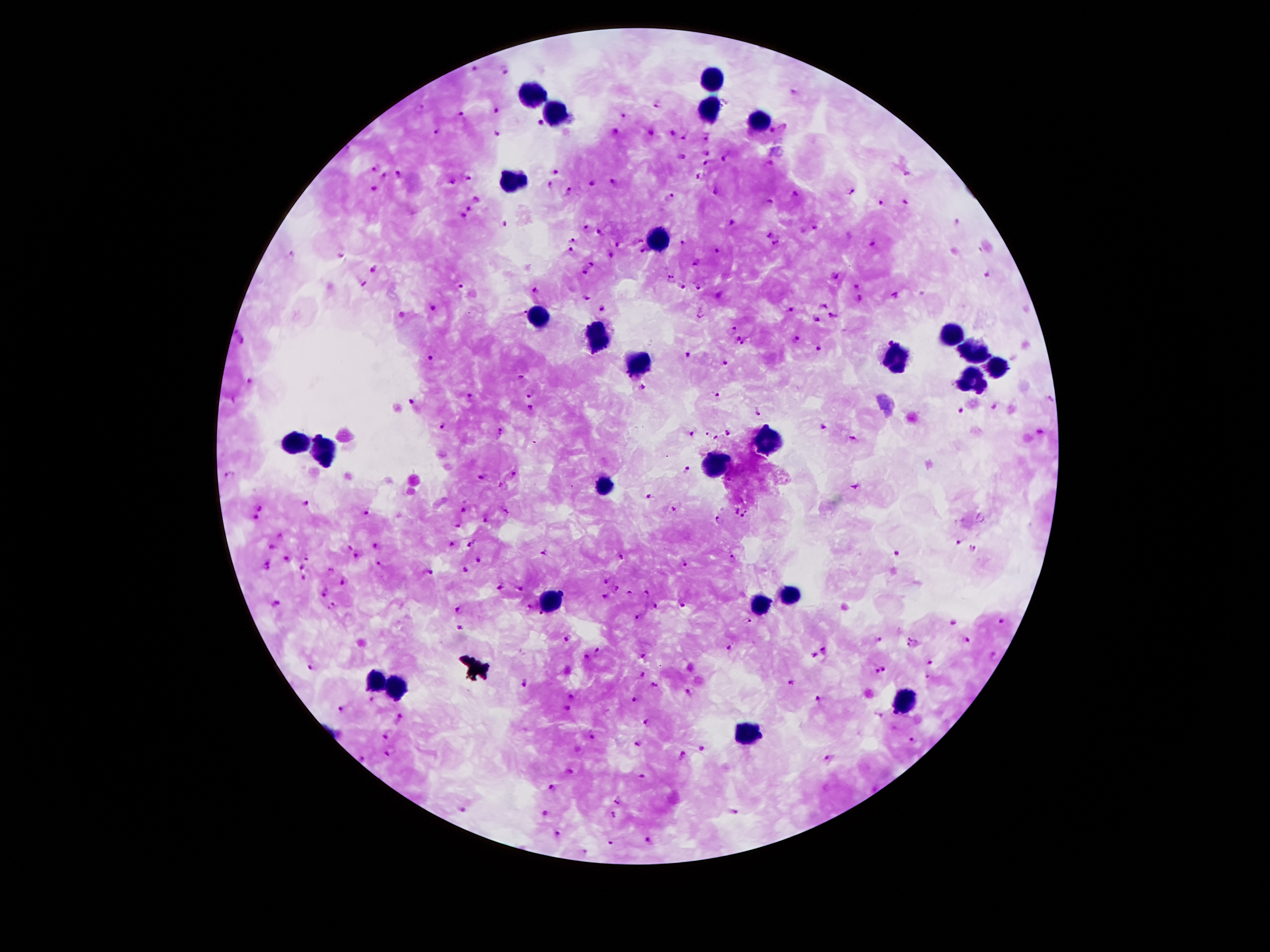 Image is 1270×952 pixels. 100x magnification. Patient malaria status: positive for Plasmodium falciparum. Thick blood film. Photographed through the microscope eyepiece with a smartphone camera. Single field of view. Giemsa-stained preparation.